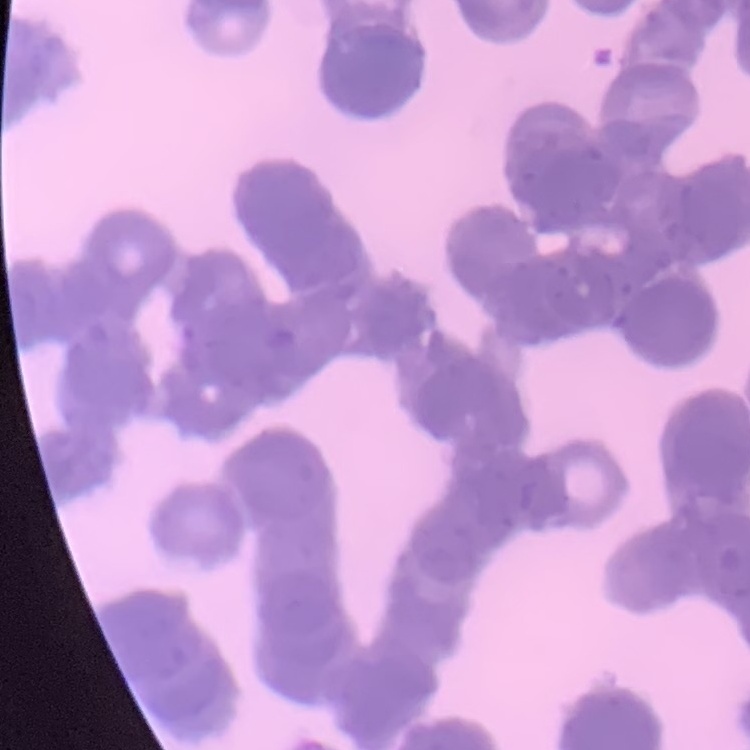

Summary:
  - Erythrocyte morphology: rouleaux formation
  - Preparation: thin peripheral smear
  - Stain: Field's or Giemsa
  - Image type: square crop of a larger photomicrograph